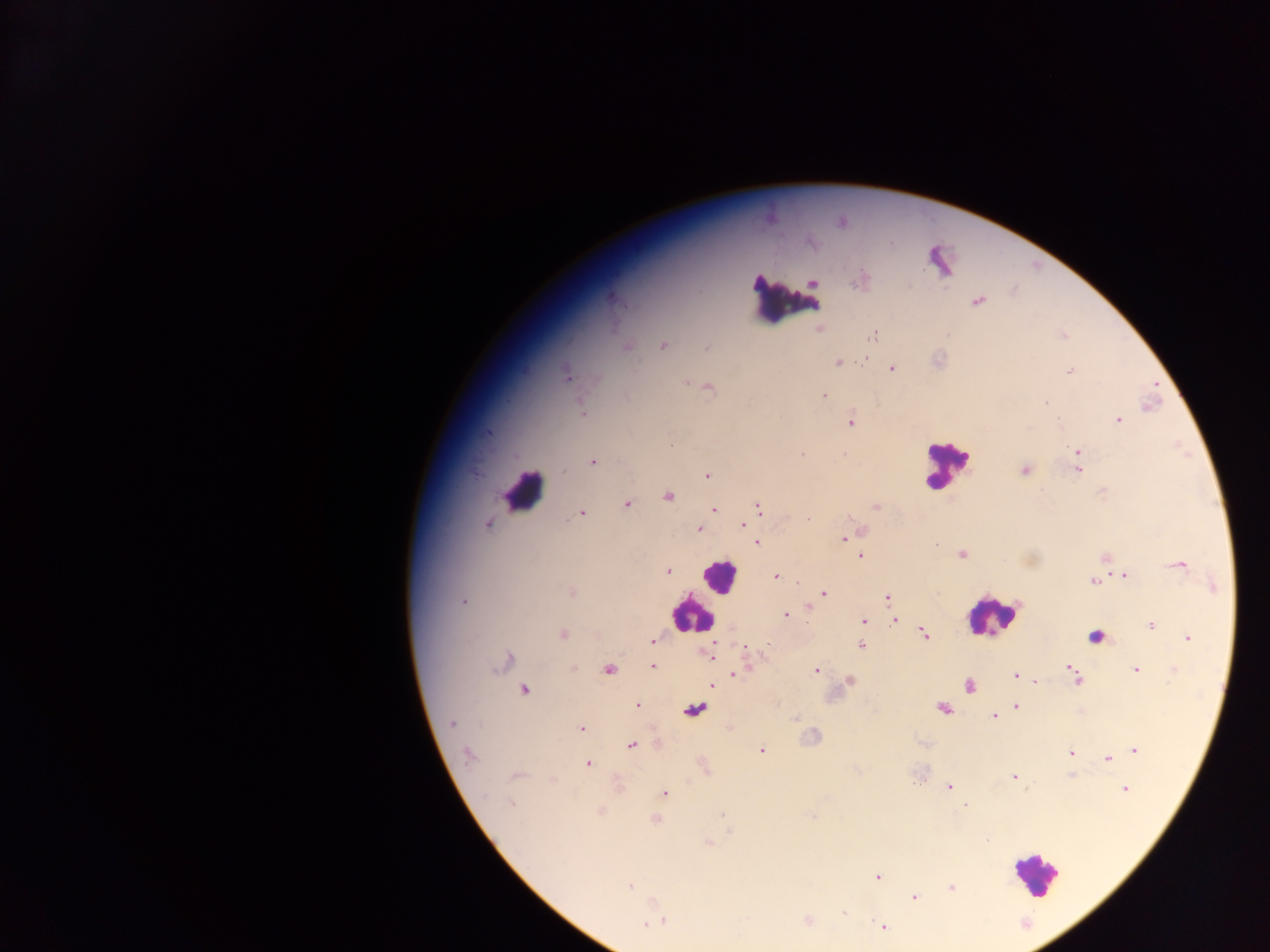
Approximate centers as {x, y} in pixels. Plasmodium parasite locations: {813, 283}, {612, 298}, {977, 301}, {820, 328}, {874, 334}, {662, 345}, {626, 347}, {707, 347}, {863, 360}, {837, 362}, {891, 368}, {1070, 370}, {567, 376}, {686, 383}, {707, 386}, {823, 396}, {1045, 401}, {582, 413}, {1118, 419}, {850, 420}, {488, 432}, {1077, 450}, {802, 454}, {844, 454}, {592, 462}, {1078, 469}, {1025, 470}, {707, 474}, {667, 495}, {626, 503}, {758, 507}, {875, 507}, {714, 510}, {581, 513}, {487, 525}, {743, 525}, {698, 529}, {844, 537}, {757, 543}, {934, 543}, {962, 554}, {860, 555}, {1105, 557}, {1178, 564}, {667, 570}, {1124, 575}, {775, 576}, {1093, 581}, {572, 592}, {823, 592}, {888, 597}, {464, 600}, {807, 608}, {786, 615}, {863, 620}, {894, 620}, {1151, 624}, {562, 634}, {924, 634}, {1187, 638}, {653, 641}, {861, 645}, {709, 654}, {503, 661}, {653, 666}, {1069, 668}, {574, 669}, {608, 669}, {815, 670}, {1136, 670}, {1173, 670}, {735, 674}, {1015, 676}, {1075, 678}, {1035, 680}, {849, 681}, {970, 685}, {711, 686}, {523, 690}, {637, 704}, {1015, 706}, {942, 708}, {693, 709}, {994, 716}, {452, 723}, {729, 726}, {581, 728}, {631, 745}, {1134, 749}, {761, 750}, {1071, 753}, {468, 755}, {1106, 758}, {588, 764}, {704, 766}, {1072, 774}, {517, 775}, {1013, 777}, {921, 779}, {618, 784}, {948, 787}, {1124, 788}, {663, 793}, {510, 803}, {965, 805}, {600, 812}, {722, 814}, {812, 817}, {655, 819}, {708, 843}, {877, 876}, {629, 885}, {951, 887}, {914, 898}, {844, 913}, {659, 917}, {807, 921}, {648, 922}, {883, 927}. Leukocyte locations: {785, 300}, {945, 465}, {523, 492}, {720, 576}, {693, 614}, {993, 614}, {1095, 636}, {1037, 874}. Thick blood smear. Single field of view. Image is 1270×952 pixels. Photographed through a microscope with a mobile-phone camera. Collected in Ghana.